State which parasite is depicted.
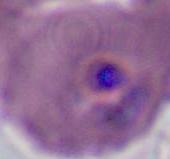
Plasmodium.

Micrograph. 400x or 1000x magnification.